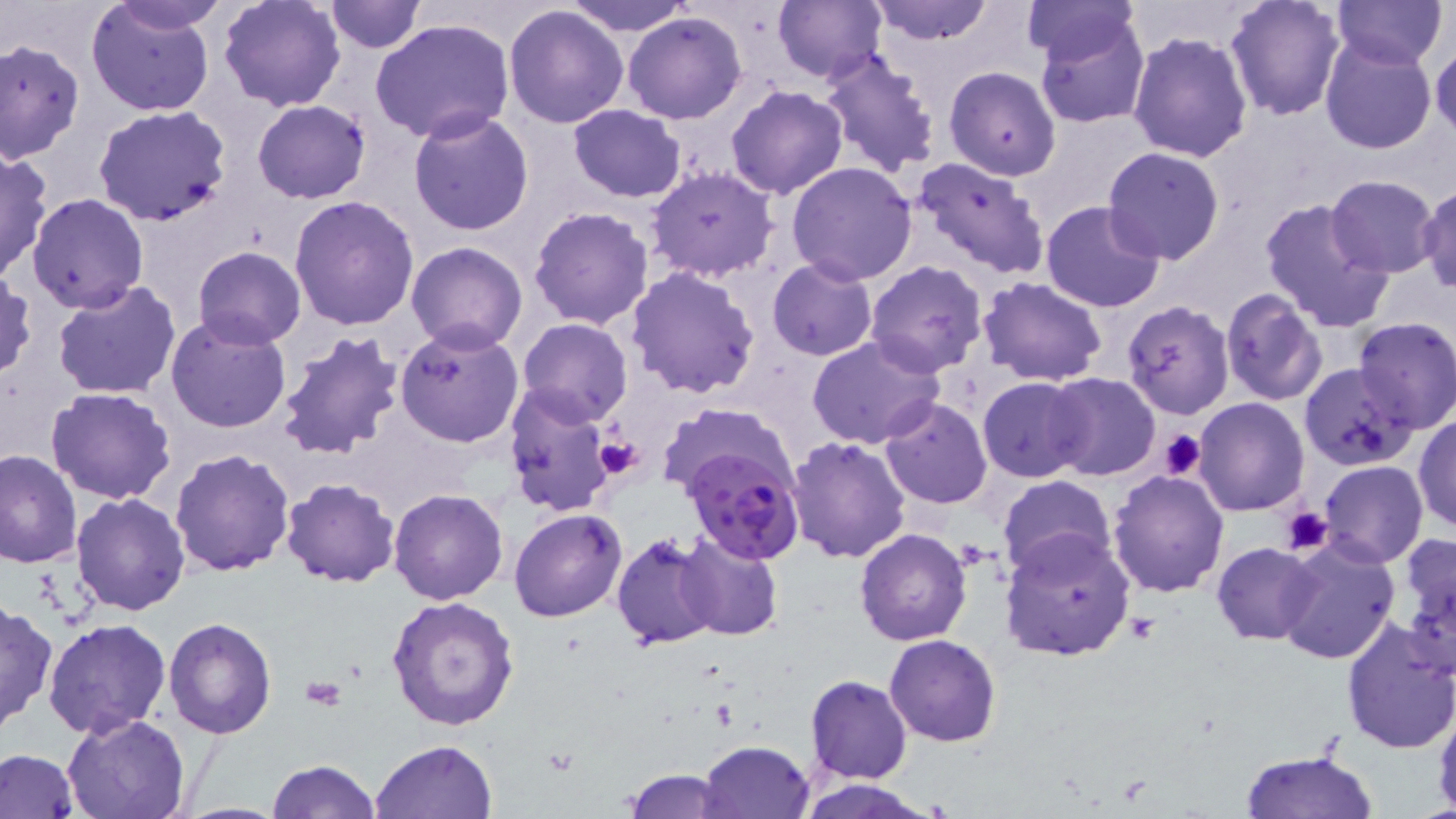

slide_level_diagnosis: Plasmodium falciparum
stain: May-Grünwald-Giemsa
uninfected_red_blood_cell_locations: 'approximate bounding boxes as [x1, y1, x2, y2] in pixels: [104, 0, 233, 34], [217, 0, 347, 112], [323, 0, 423, 53], [570, 0, 693, 36], [774, 0, 887, 85], [869, 0, 993, 44], [1224, 0, 1345, 120], [1333, 0, 1448, 69], [1021, 1, 1139, 67], [86, 2, 215, 115], [504, 4, 630, 129], [624, 12, 747, 125], [1033, 13, 1151, 130], [370, 16, 515, 145], [1128, 30, 1253, 161], [1319, 37, 1436, 155], [1430, 37, 1455, 141], [0, 39, 85, 165], [820, 47, 943, 177], [944, 66, 1061, 180], [726, 85, 849, 200], [252, 99, 370, 203], [92, 104, 233, 227], [568, 104, 686, 202], [408, 110, 534, 235], [1101, 147, 1226, 265], [0, 148, 52, 282], [911, 158, 1051, 282], [786, 161, 918, 284], [645, 166, 780, 281], [1325, 174, 1441, 277], [1417, 185, 1456, 293], [26, 194, 149, 314], [290, 195, 420, 330], [1260, 196, 1393, 333], [1041, 198, 1165, 312], [529, 207, 655, 330], [406, 241, 526, 352], [193, 246, 306, 348], [767, 259, 877, 360], [866, 260, 988, 377], [627, 265, 761, 398], [1, 272, 36, 381], [978, 276, 1108, 386], [52, 279, 183, 402], [1220, 287, 1328, 405], [53, 296, 292, 419], [1122, 301, 1234, 419], [165, 313, 293, 436], [1353, 317, 1456, 430], [518, 318, 633, 426], [395, 324, 523, 447], [275, 329, 405, 463], [807, 335, 944, 448], [1299, 364, 1418, 471], [1044, 372, 1160, 481], [979, 376, 1089, 482], [46, 386, 177, 504], [504, 387, 616, 517], [880, 397, 992, 508], [1193, 398, 1309, 514], [657, 403, 798, 500], [1414, 413, 1456, 535], [786, 436, 910, 563], [168, 447, 293, 576], [0, 450, 82, 569], [1319, 460, 1428, 568], [1109, 469, 1229, 597], [998, 475, 1116, 581], [279, 478, 400, 586], [388, 489, 508, 605], [71, 492, 190, 616], [509, 508, 628, 622], [855, 529, 972, 646], [1000, 532, 1135, 663], [610, 533, 721, 651], [675, 533, 783, 641], [1276, 536, 1401, 665], [1397, 536, 1455, 676], [1213, 543, 1323, 644], [387, 597, 520, 730], [0, 598, 57, 735], [165, 617, 277, 738], [43, 618, 171, 739], [1338, 618, 1455, 753], [885, 634, 1000, 747], [805, 675, 913, 784], [1433, 699, 1456, 819], [63, 714, 189, 819], [369, 739, 497, 819], [699, 740, 814, 818], [0, 749, 81, 819], [1240, 749, 1378, 819], [267, 759, 380, 818], [621, 768, 736, 818], [800, 779, 934, 818]'
preparation: thin blood smear
platelet_locations: 'approximate bounding boxes as [x1, y1, x2, y2] in pixels: [1158, 430, 1206, 482], [592, 435, 647, 482], [1279, 507, 1334, 555], [300, 677, 346, 711]'
image_size: 1456×819 pixels
field_of_view: single
plasmodium_falciparum_infected_red_blood_cell_locations: 'approximate bounding boxes as [x1, y1, x2, y2] in pixels: [680, 444, 806, 565]'
magnification: 1000x
modality: light microscopy